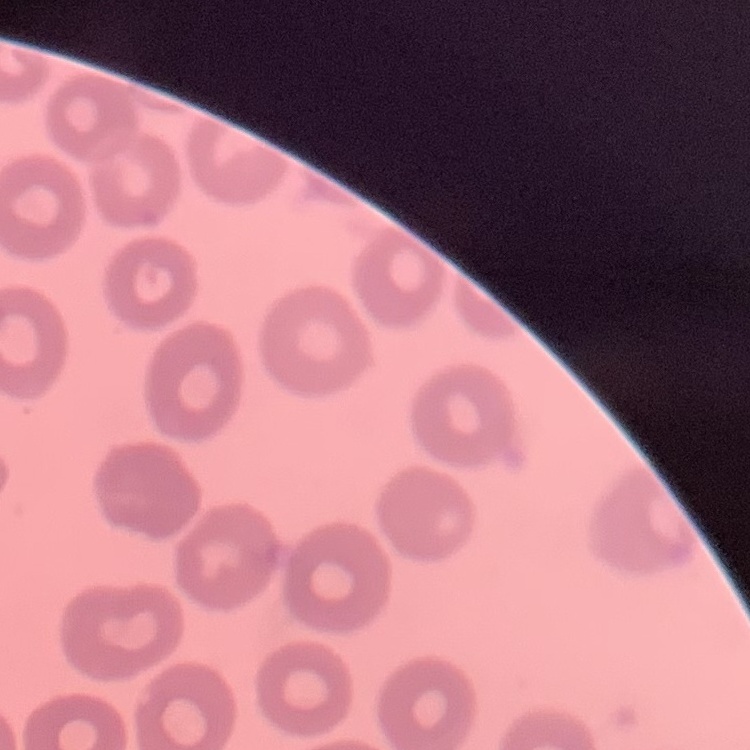

The red blood cells show no rouleaux formation. One tile cut from a larger photomicrograph. Thin blood film. Field's or Giemsa stain.